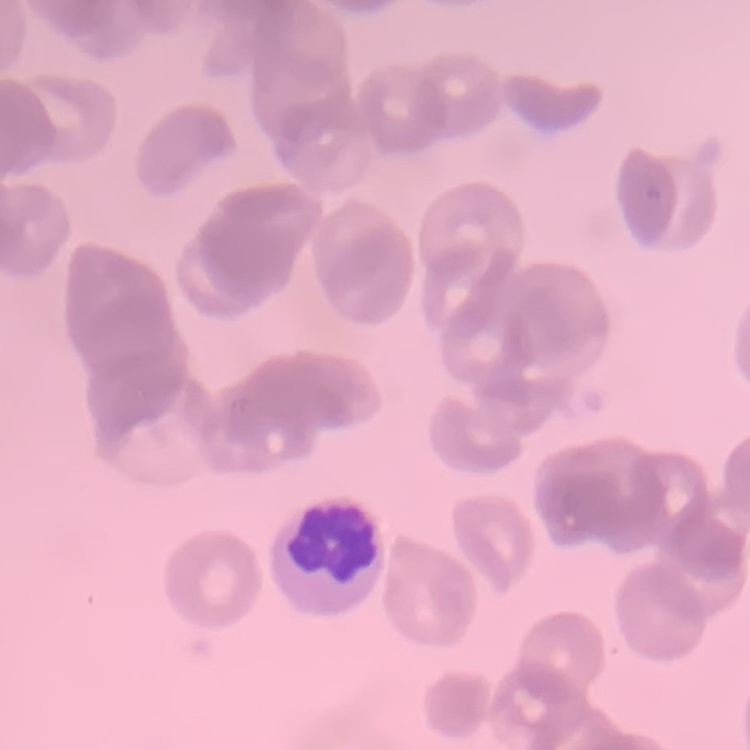

Summary:
  - Erythrocyte morphology: rouleaux formation
  - Stain: Field's or Giemsa
  - Preparation: thin blood smear
  - Image type: one tile cut from a larger photomicrograph